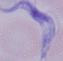
Micrograph. A trypanosome is shown. 1000x magnification.